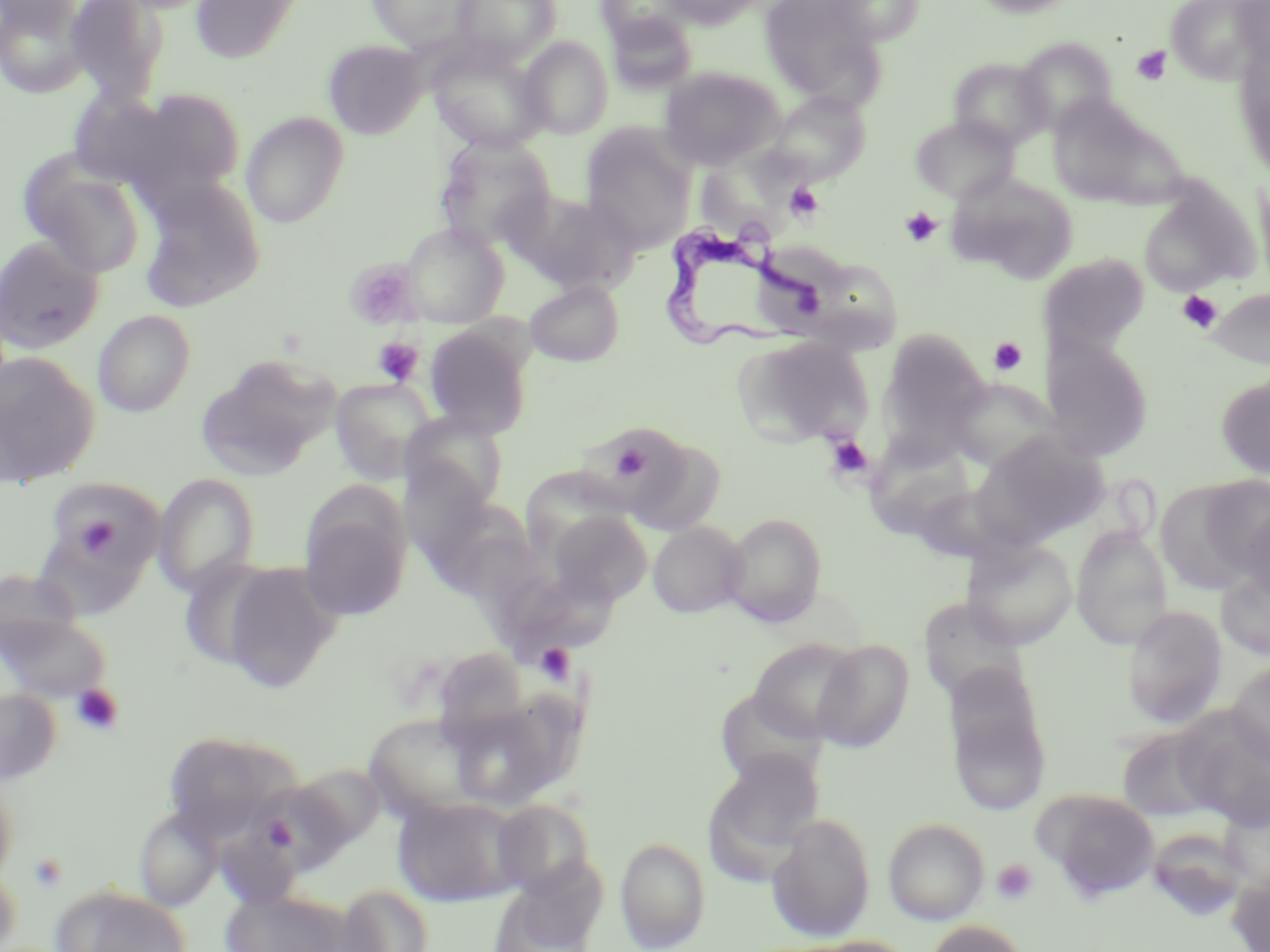

slide-level diagnosis = Trypanosoma brucei
field of view = one of a larger specimen
stain = May-Grünwald-Giemsa
image size = 1270×952 pixels
preparation = thin blood smear
magnification = 1000x
platelet locations = approximate bounding boxes as [x1, y1, x2, y2] in pixels: [1131, 46, 1172, 86], [785, 182, 824, 221], [900, 207, 943, 247], [345, 259, 422, 330], [1177, 290, 1222, 332], [372, 337, 423, 386], [987, 337, 1028, 376], [825, 435, 874, 481], [610, 440, 652, 482], [73, 513, 125, 560], [534, 643, 575, 684], [71, 684, 124, 736], [29, 853, 68, 891], [991, 858, 1039, 905]
uninfected red blood cell locations = approximate bounding boxes as [x1, y1, x2, y2] in pixels: [65, 0, 171, 105], [189, 0, 305, 64], [365, 0, 482, 51], [451, 0, 562, 65], [597, 0, 693, 49], [661, 0, 761, 29], [760, 0, 883, 103], [822, 0, 927, 46], [970, 0, 1079, 17], [1167, 0, 1264, 83], [1, 1, 94, 99], [1233, 1, 1270, 64], [606, 12, 698, 94], [517, 36, 613, 139], [1015, 37, 1118, 134], [427, 39, 549, 153], [324, 40, 428, 139], [1236, 46, 1270, 179], [948, 57, 1053, 150], [660, 67, 783, 169], [103, 89, 247, 199], [768, 92, 871, 185], [1047, 96, 1159, 205], [241, 112, 349, 228], [910, 115, 1019, 204], [580, 124, 697, 251], [434, 135, 557, 251], [18, 154, 147, 279], [699, 156, 810, 238], [948, 173, 1080, 284], [1254, 174, 1270, 291], [137, 176, 266, 312], [1137, 182, 1258, 295], [520, 192, 642, 294], [400, 222, 509, 327], [0, 235, 105, 354], [1039, 254, 1149, 359], [825, 262, 902, 358], [524, 279, 624, 366], [1209, 288, 1269, 370], [92, 309, 196, 417], [425, 323, 533, 439], [878, 328, 991, 456], [735, 335, 873, 447], [1042, 340, 1154, 462], [0, 351, 99, 486], [196, 354, 339, 480], [1216, 375, 1270, 479], [329, 378, 437, 486], [946, 378, 1057, 473], [401, 412, 509, 511], [620, 432, 727, 535], [972, 433, 1108, 546], [864, 434, 974, 540], [521, 465, 632, 559], [153, 473, 260, 597], [1198, 475, 1270, 581], [44, 476, 166, 579], [423, 501, 532, 594], [299, 504, 411, 621], [1241, 508, 1270, 605], [546, 510, 652, 606], [722, 513, 827, 627], [647, 521, 750, 618], [1070, 525, 1173, 648], [962, 537, 1078, 650], [176, 557, 283, 673], [217, 561, 342, 693], [1, 567, 86, 656], [1217, 567, 1270, 661], [503, 583, 612, 665], [918, 598, 1028, 704], [1123, 604, 1227, 729], [1, 610, 112, 704], [748, 639, 862, 741], [813, 640, 913, 753], [431, 646, 531, 741], [1228, 662, 1270, 765], [0, 687, 61, 785], [715, 688, 825, 787], [946, 691, 1050, 817], [446, 697, 569, 809], [1174, 711, 1270, 830], [364, 713, 491, 819], [1116, 726, 1221, 822], [163, 732, 285, 841], [705, 751, 825, 873], [292, 763, 385, 850], [0, 766, 18, 886], [247, 780, 351, 874], [1034, 788, 1160, 899], [393, 796, 525, 906], [491, 799, 596, 898], [134, 808, 222, 911], [767, 813, 876, 941], [884, 819, 989, 924], [1145, 828, 1249, 923], [614, 836, 711, 951], [491, 863, 607, 952], [0, 865, 22, 952], [1227, 870, 1270, 952], [335, 883, 434, 952], [51, 885, 194, 951], [220, 888, 351, 952], [925, 920, 1031, 952], [792, 936, 916, 952]
modality = light microscopy
Trypanosoma brucei locations = approximate bounding boxes as [x1, y1, x2, y2] in pixels: [656, 221, 829, 347]